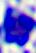

identification = white blood cell
modality = micrograph
magnification = 400x